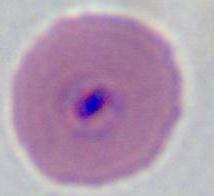

Micrograph. A Plasmodium parasite is shown. 400x or 1000x magnification.